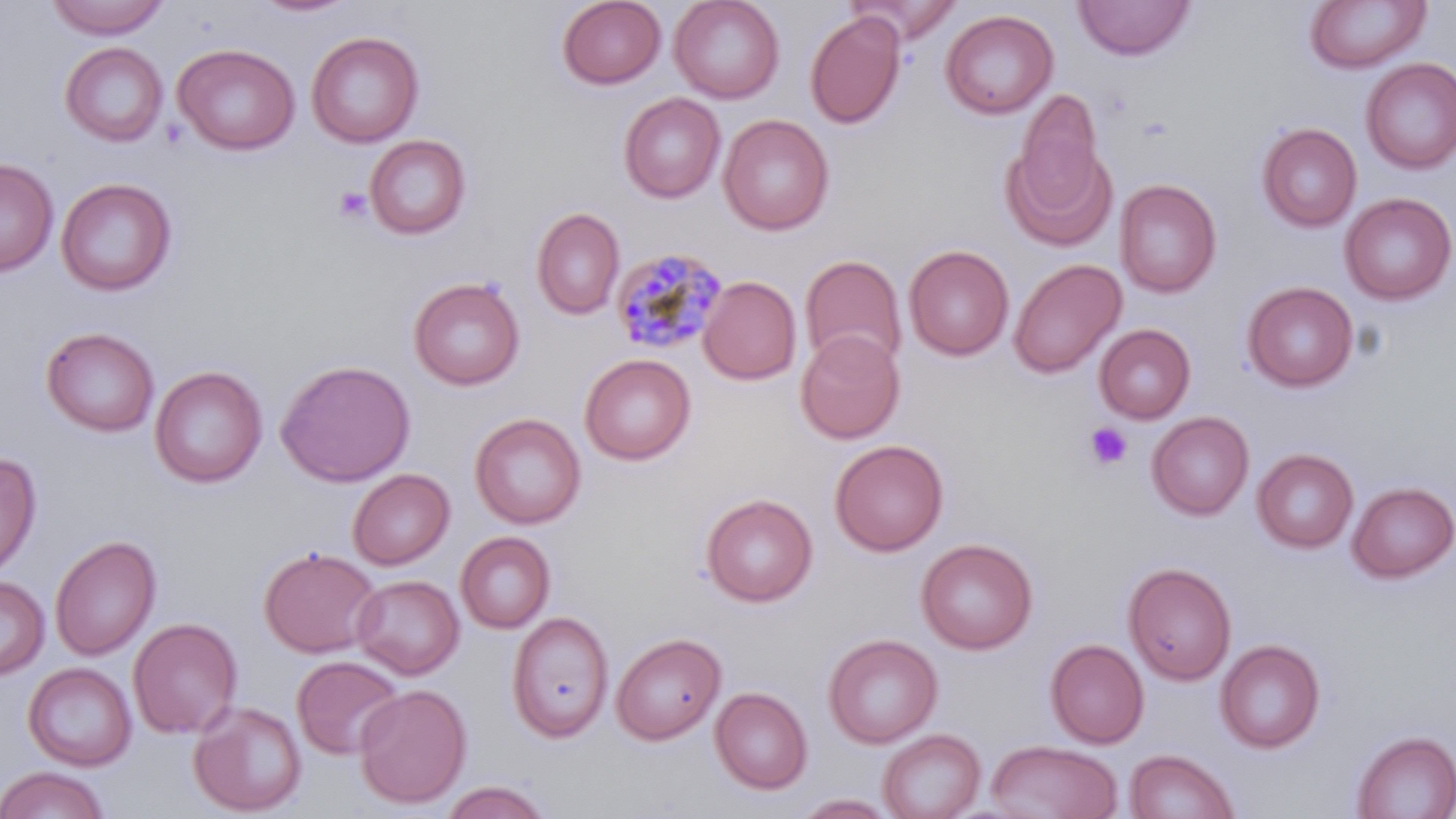 Approximate bounding boxes as [x1, y1, x2, y2] in pixels. Plasmodium malariae-infected red blood cell locations: [610, 246, 728, 355]. Platelet locations: [333, 187, 372, 223], [1084, 422, 1133, 471]. Uninfected red blood cell locations: [557, 0, 667, 89], [669, 0, 784, 103], [848, 0, 964, 46], [1073, 0, 1195, 61], [1305, 0, 1430, 73], [44, 1, 171, 40], [250, 1, 359, 19], [940, 9, 1058, 120], [805, 11, 905, 129], [306, 30, 424, 148], [60, 42, 168, 147], [172, 43, 300, 155], [1361, 59, 1456, 174], [1014, 89, 1104, 208], [618, 92, 725, 203], [718, 114, 835, 235], [1257, 123, 1361, 232], [364, 134, 471, 240], [1001, 138, 1116, 252], [0, 157, 59, 277], [55, 177, 178, 297], [1115, 178, 1222, 298], [1339, 193, 1455, 305], [532, 207, 624, 319], [904, 244, 1014, 361], [801, 254, 907, 371], [1009, 258, 1125, 378], [699, 275, 801, 385], [408, 277, 525, 391], [1243, 281, 1358, 392], [1094, 324, 1196, 424], [41, 326, 160, 437], [795, 330, 905, 444], [579, 353, 696, 465], [276, 359, 415, 487], [149, 365, 268, 488], [1147, 411, 1254, 520], [469, 412, 586, 529], [830, 439, 948, 556], [1252, 448, 1359, 553], [0, 450, 42, 579], [348, 468, 455, 569], [1347, 481, 1456, 583], [700, 493, 817, 606], [456, 531, 556, 633], [50, 534, 161, 661], [916, 537, 1038, 654], [259, 546, 381, 657], [1123, 561, 1237, 685], [352, 574, 465, 679], [0, 575, 50, 679], [506, 611, 614, 743], [128, 617, 243, 738], [612, 632, 726, 745], [824, 633, 942, 748], [1046, 638, 1149, 748], [1215, 639, 1325, 753], [292, 655, 405, 760], [23, 662, 137, 771], [354, 683, 471, 808], [710, 686, 812, 795], [188, 699, 308, 816], [879, 728, 985, 819], [1352, 730, 1456, 819], [985, 740, 1123, 819], [1124, 749, 1240, 819], [0, 766, 111, 818], [437, 780, 554, 819], [795, 794, 897, 818]. Slide-level diagnosis: Plasmodium malariae. Single field of view. Image is 1456×819 pixels. Light microscopy. 1000x magnification. May-Grünwald-Giemsa stain. Thin blood smear.